Identify the parasite.
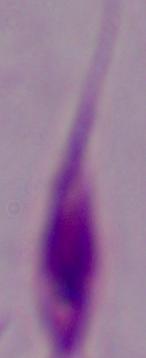

This is Leishmania.

magnification = 1000x
modality = micrograph